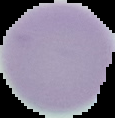
Summary:
  - Image type: cell region segmented out of the field of view; surrounding area masked to black
  - Image size: 115×118 pixels
  - Malaria status: uninfected
  - Preparation: thin blood smear